Classify this cell by malaria status.
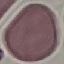

It is uninfected.

Summary:
  - Stain: Giemsa
  - Image type: automatically extracted cell patch, resized to 64 × 64 pixels
  - Capture: smartphone camera at the microscope eyepiece
  - Preparation: thin blood smear